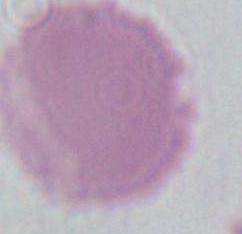

A red blood cell is seen. Captured at 1000x magnification. Micrograph.